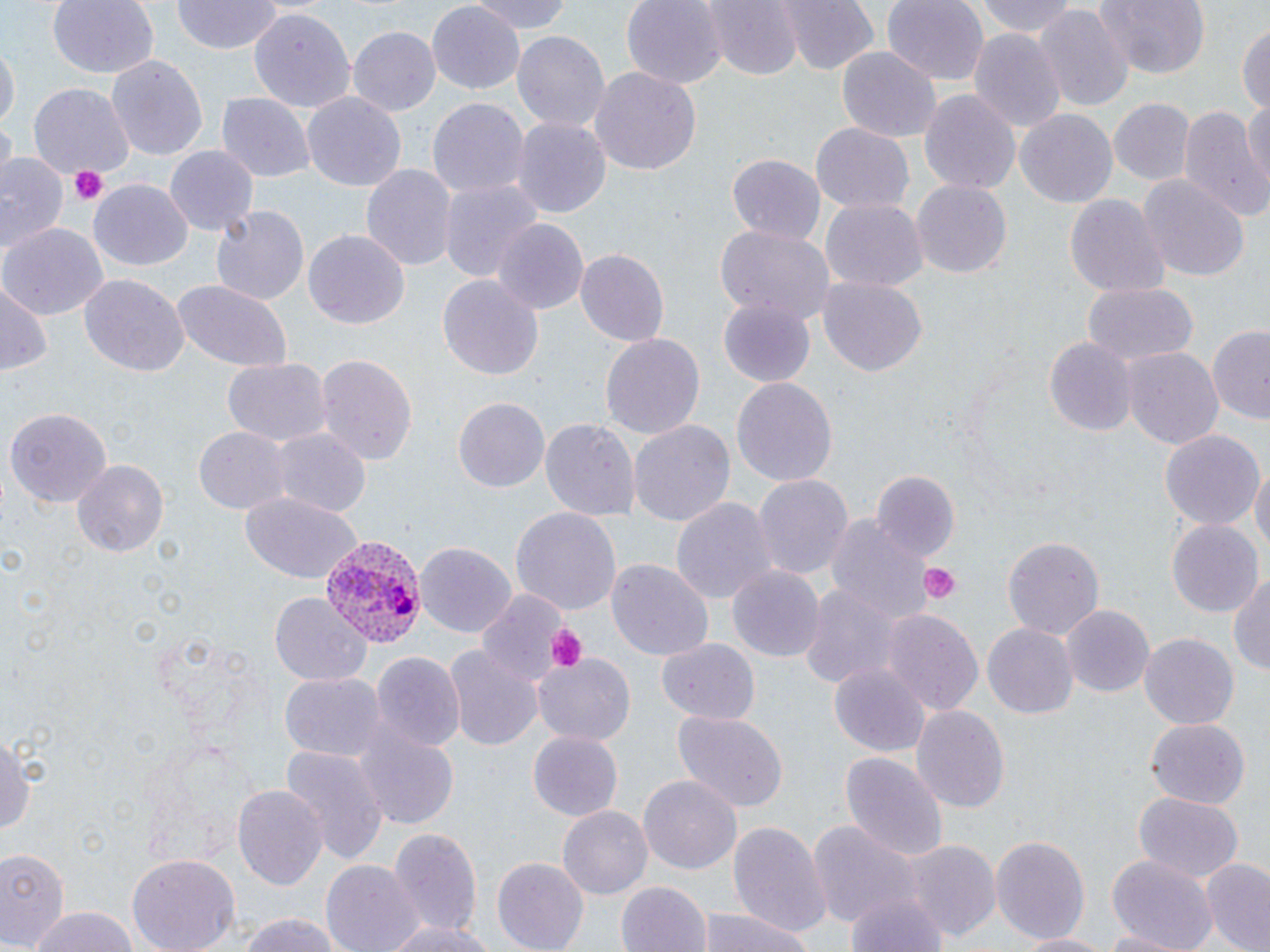
Summary:
  - Coordinate format: approximate bounding boxes as (x1,y1)-(x2,y2) corner pairs in pixels
  - Uninfected red blood cell locations: (46,0)-(159,80), (468,0)-(572,33), (621,0)-(725,91), (706,0)-(802,81), (785,0)-(880,75), (881,0)-(988,86), (972,0)-(1081,38), (1094,0)-(1210,76), (171,1)-(280,55), (427,5)-(524,94), (1037,5)-(1132,115), (249,8)-(356,112), (1237,19)-(1270,120), (349,26)-(440,116), (513,29)-(610,132), (969,30)-(1065,131), (0,45)-(17,135), (835,45)-(940,144), (106,54)-(209,164), (588,66)-(700,179), (30,82)-(134,177), (918,88)-(1021,194), (301,91)-(407,192), (217,94)-(312,184), (1107,96)-(1194,185), (427,98)-(528,202), (1243,101)-(1270,201), (1179,104)-(1264,221), (1015,111)-(1118,207), (513,116)-(612,222), (2,120)-(14,180), (811,124)-(914,217), (165,146)-(259,237), (727,154)-(826,245), (0,155)-(65,256), (360,164)-(455,275), (1139,176)-(1250,281), (438,177)-(543,282), (911,180)-(1011,280), (90,181)-(191,270), (1065,192)-(1168,299), (822,201)-(928,290), (210,202)-(310,305), (494,218)-(589,314), (0,222)-(108,319), (716,224)-(834,324), (304,227)-(409,329), (576,248)-(669,346), (80,273)-(188,379), (438,274)-(544,381), (819,274)-(926,377), (168,277)-(294,372), (1080,281)-(1199,368), (1,282)-(50,378), (717,294)-(818,388), (1208,325)-(1270,424), (600,333)-(704,438), (1044,336)-(1136,436), (1122,348)-(1222,449), (314,353)-(417,465), (221,357)-(331,448), (731,377)-(838,487), (453,394)-(549,491), (6,407)-(113,506), (629,417)-(734,527), (540,418)-(637,525), (195,427)-(290,512), (1158,428)-(1262,530), (273,429)-(370,518), (72,458)-(168,559), (1249,459)-(1269,561), (752,473)-(852,581), (872,473)-(960,564), (239,486)-(363,583), (672,496)-(774,611), (510,506)-(621,616), (825,513)-(938,627), (1167,520)-(1262,617), (1001,535)-(1102,640), (416,542)-(514,637), (606,557)-(714,662), (728,564)-(823,663), (1230,569)-(1270,681), (798,582)-(902,688), (270,592)-(371,688), (1063,606)-(1155,697), (883,607)-(983,717), (982,621)-(1078,719), (1139,635)-(1237,727), (655,638)-(760,723), (444,645)-(542,751), (372,651)-(464,751), (533,653)-(634,747), (830,664)-(928,756), (281,675)-(383,759), (911,704)-(1010,815), (672,708)-(789,813), (1146,718)-(1250,808), (354,724)-(457,829), (0,726)-(35,846), (528,732)-(623,822), (282,745)-(387,862), (840,750)-(947,865), (639,773)-(742,872), (231,783)-(327,893), (1132,793)-(1243,883), (558,804)-(652,900), (727,819)-(829,934), (810,822)-(922,939), (388,827)-(482,935), (989,834)-(1090,943), (896,839)-(1001,943), (0,845)-(69,950), (1105,855)-(1218,950), (127,856)-(239,952), (491,856)-(588,952), (1201,858)-(1270,951), (322,859)-(425,952), (617,878)-(710,952), (844,884)-(950,952), (697,905)-(818,952), (24,907)-(140,952), (232,911)-(351,952), (382,917)-(497,952), (1095,927)-(1196,952), (1014,930)-(1112,951)
  - Platelet locations: (70,166)-(106,205), (920,562)-(960,605), (542,621)-(588,672)
  - Plasmodium vivax-infected red blood cell locations: (319,534)-(425,650)
  - Slide-level diagnosis: Plasmodium vivax
  - Preparation: thin blood smear
  - Magnification: 1000x
  - Image size: 1270×952 pixels
  - Modality: optical microscopy
  - Field of view: one of a larger specimen
  - Stain: May-Grünwald-Giemsa